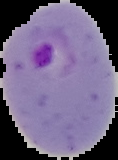

The area outside the segmented cell region is set to black. Result: malaria parasites detected. From a thin blood film. Image is 118×160 pixels.